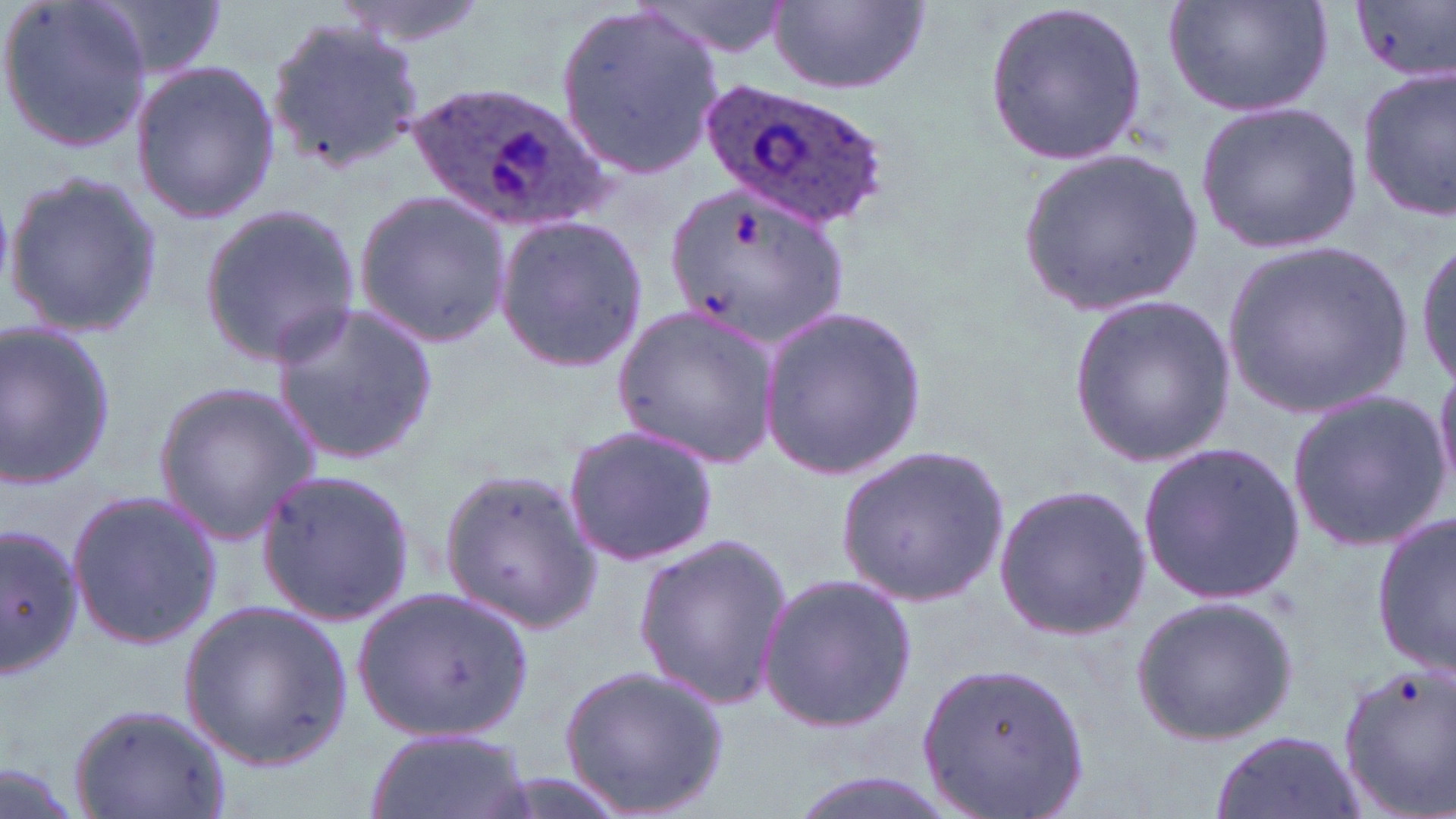 Approximate bounding boxes as (x1, y1, x2, y2) in pixels. Plasmodium ovale-infected red blood cell locations: (705, 78, 889, 230), (412, 83, 603, 233). Uninfected red blood cell locations: (0, 0, 154, 155), (84, 0, 229, 77), (333, 0, 493, 49), (636, 0, 794, 62), (767, 0, 933, 97), (983, 0, 1147, 169), (1161, 0, 1337, 117), (1350, 0, 1456, 83), (552, 3, 724, 181), (265, 18, 424, 170), (129, 59, 282, 226), (1355, 67, 1456, 221), (1193, 102, 1364, 254), (1015, 149, 1204, 314), (4, 171, 164, 338), (664, 177, 849, 345), (350, 187, 512, 351), (198, 199, 363, 367), (493, 214, 650, 373), (1412, 232, 1456, 396), (1223, 240, 1420, 415), (1067, 295, 1236, 466), (269, 302, 439, 465), (760, 303, 928, 481), (611, 304, 782, 470), (0, 321, 117, 491), (1433, 362, 1456, 498), (152, 382, 320, 542), (1287, 392, 1451, 551), (561, 419, 722, 568), (1137, 440, 1306, 601), (834, 443, 1010, 605), (254, 466, 416, 625), (438, 468, 600, 633), (992, 484, 1151, 639), (65, 486, 223, 651), (1374, 511, 1454, 674), (1, 522, 82, 681), (631, 533, 794, 710), (758, 572, 919, 734), (358, 584, 535, 745), (1129, 595, 1300, 744), (179, 601, 353, 770), (917, 659, 1092, 818), (556, 660, 735, 819), (1338, 665, 1456, 816), (67, 702, 234, 819), (361, 727, 535, 819), (1209, 729, 1363, 819), (0, 756, 84, 819), (774, 771, 966, 819). Slide-level diagnosis: Plasmodium ovale. Image is 1456×819 pixels. Thin blood smear. Captured at 1000x magnification. Single field of view. Optical microscopy. May-Grünwald-Giemsa-stained preparation.